State which parasite is depicted.
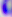
This is Toxoplasma gondii.

modality = micrograph
magnification = 400x